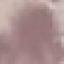

Result: no malaria parasites detected. Acquired by smartphone through the microscope eyepiece. Thin blood smear. Giemsa stain. Automatically extracted cell patch, resized to 64 × 64 pixels.